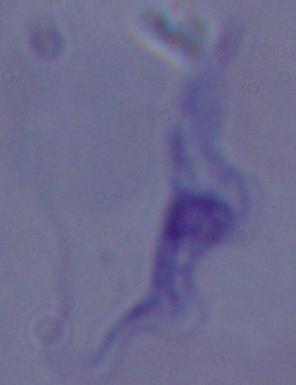
Summary:
  - Magnification: 1000x
  - Identification: trypanosome
  - Modality: micrograph